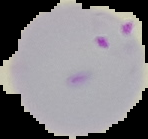
Summary:
  - Preparation: thin blood smear
  - Image size: 148×139 pixels
  - Image type: segmented cell region on a black background
  - Malaria status: parasitized